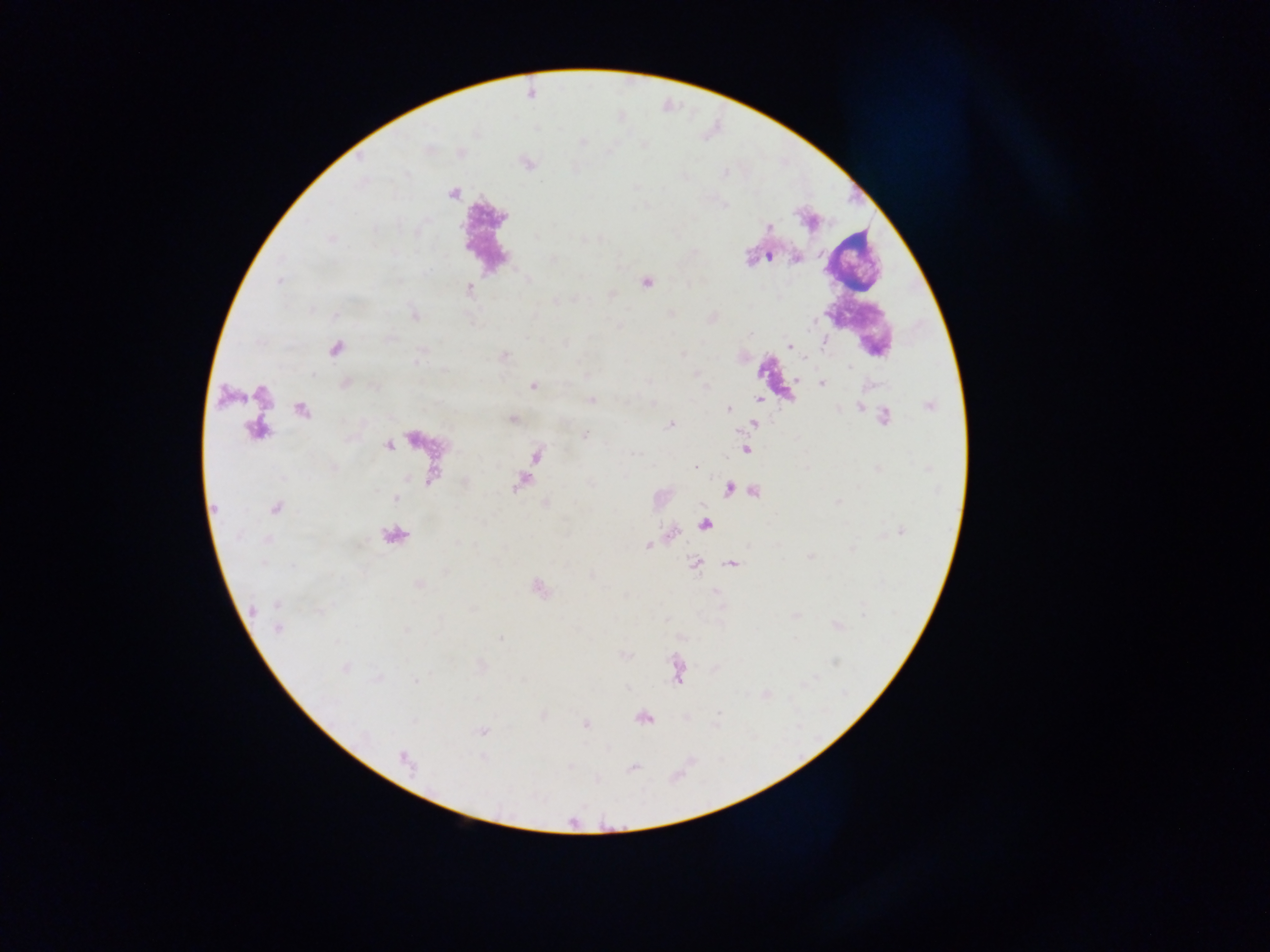
Photographed through a microscope with a mobile-phone camera. Single field of view. Thick blood film. Image is 1270×952 pixels. Collected in Ghana.